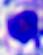
A white blood cell is shown. Photomicrograph. 400x magnification.